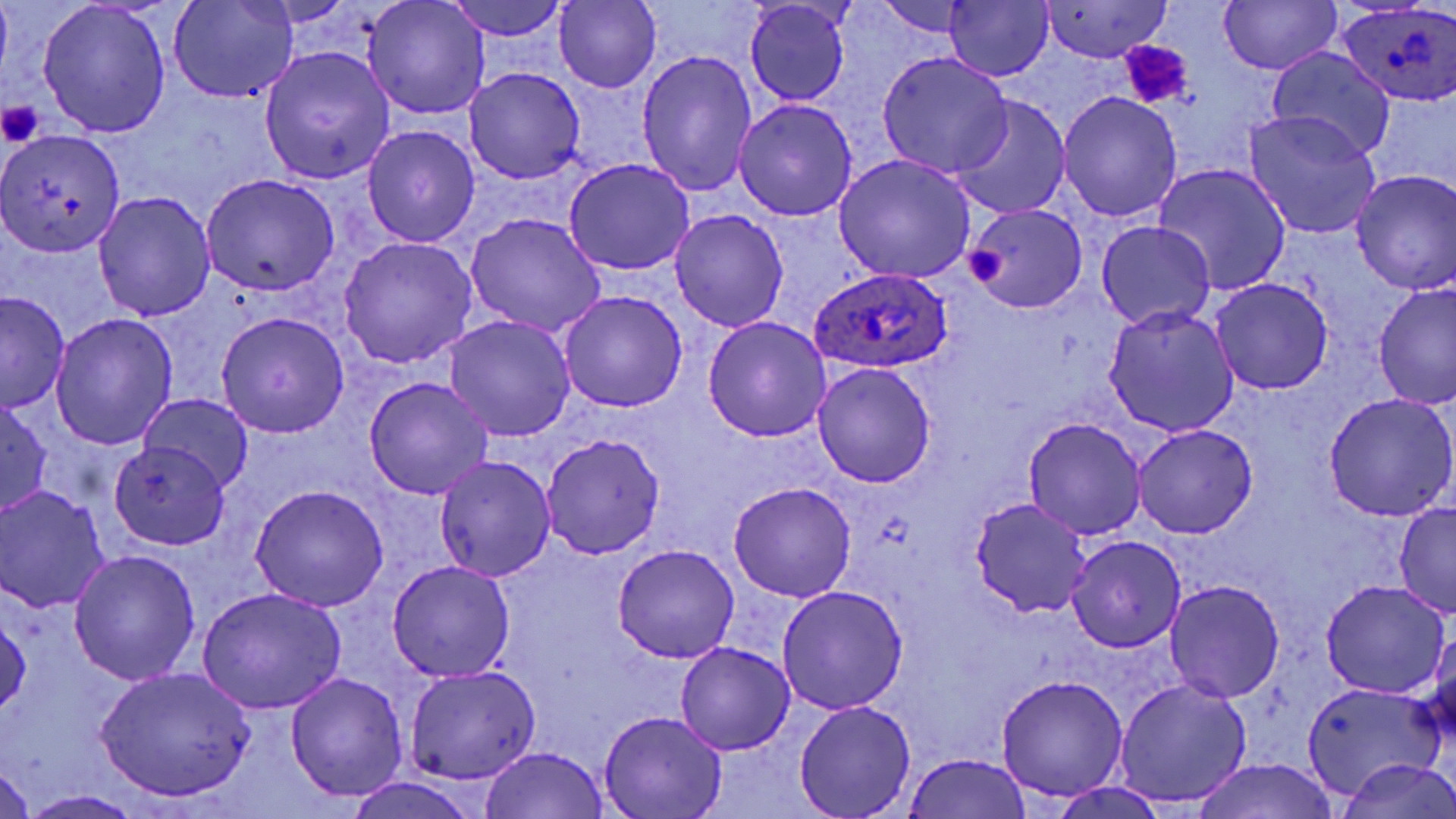

Approximate bounding boxes as (x1, y1, x2, y2) in pixels. Platelet locations: (1118, 42, 1190, 109), (0, 98, 46, 146), (965, 248, 1006, 284). Uninfected red blood cell locations: (170, 0, 296, 102), (363, 0, 490, 121), (553, 0, 662, 92), (1038, 0, 1172, 64), (1219, 0, 1341, 74), (443, 1, 572, 40), (744, 2, 852, 106), (874, 2, 985, 37), (37, 3, 171, 138), (942, 3, 1053, 80), (1268, 46, 1396, 162), (259, 48, 395, 183), (636, 51, 757, 198), (876, 52, 1014, 177), (464, 68, 586, 184), (1057, 93, 1182, 222), (949, 97, 1072, 220), (733, 100, 858, 221), (1247, 113, 1381, 238), (363, 124, 479, 248), (0, 129, 126, 258), (833, 154, 975, 284), (564, 159, 694, 275), (1156, 163, 1290, 294), (1350, 170, 1456, 294), (200, 174, 339, 297), (93, 190, 216, 323), (966, 204, 1087, 314), (670, 210, 789, 330), (465, 213, 607, 338), (1097, 220, 1216, 329), (339, 237, 478, 368), (1211, 278, 1334, 393), (1373, 283, 1455, 413), (558, 290, 687, 412), (0, 292, 70, 412), (1104, 307, 1239, 437), (216, 312, 349, 438), (51, 314, 177, 450), (443, 317, 576, 441), (703, 317, 832, 441), (813, 363, 935, 488), (363, 376, 493, 500), (1324, 393, 1456, 520), (0, 395, 51, 518), (139, 395, 254, 492), (1023, 417, 1147, 540), (1133, 424, 1258, 537), (540, 432, 665, 559), (109, 442, 230, 551), (434, 455, 556, 581), (727, 482, 857, 602), (249, 485, 389, 610), (0, 486, 110, 613), (968, 496, 1093, 619), (1394, 502, 1455, 617), (1067, 536, 1186, 653), (613, 544, 740, 663), (68, 548, 201, 687), (386, 560, 516, 682), (1166, 580, 1284, 702), (1321, 581, 1450, 698), (776, 587, 909, 715), (197, 588, 346, 715), (0, 604, 30, 721), (1428, 629, 1456, 750), (676, 641, 795, 754), (403, 665, 540, 785), (93, 666, 257, 800), (286, 671, 409, 802), (996, 675, 1129, 801), (1115, 678, 1251, 807), (1301, 682, 1446, 800), (794, 700, 918, 818), (600, 709, 728, 819), (480, 746, 611, 818), (902, 753, 1035, 819), (1333, 757, 1456, 818), (1188, 758, 1343, 819), (0, 759, 36, 819), (343, 778, 483, 819), (1050, 780, 1167, 819), (18, 790, 145, 818). Plasmodium ovale-infected red blood cell locations: (1340, 3, 1452, 107), (808, 269, 955, 374). Slide-level diagnosis: Plasmodium ovale. One field of a larger specimen. Thin blood smear. Captured at 1000x magnification. May-Grünwald-Giemsa stain. Image is 1456×819 pixels. Light microscopy.